Comment on the morphology of the red blood cells.
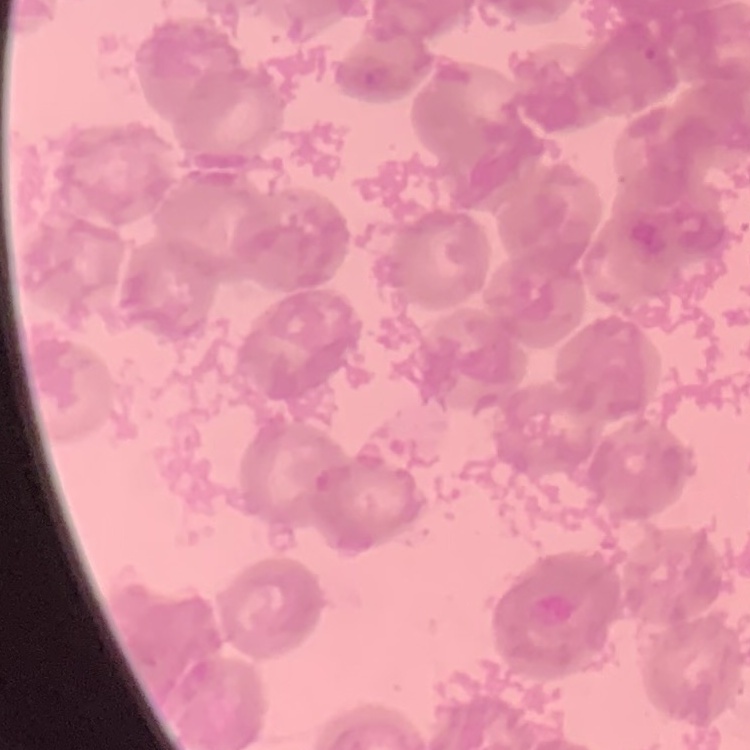
They show rouleaux formation.

stain = Field's or Giemsa
image type = square crop of a larger photomicrograph
preparation = thin blood film